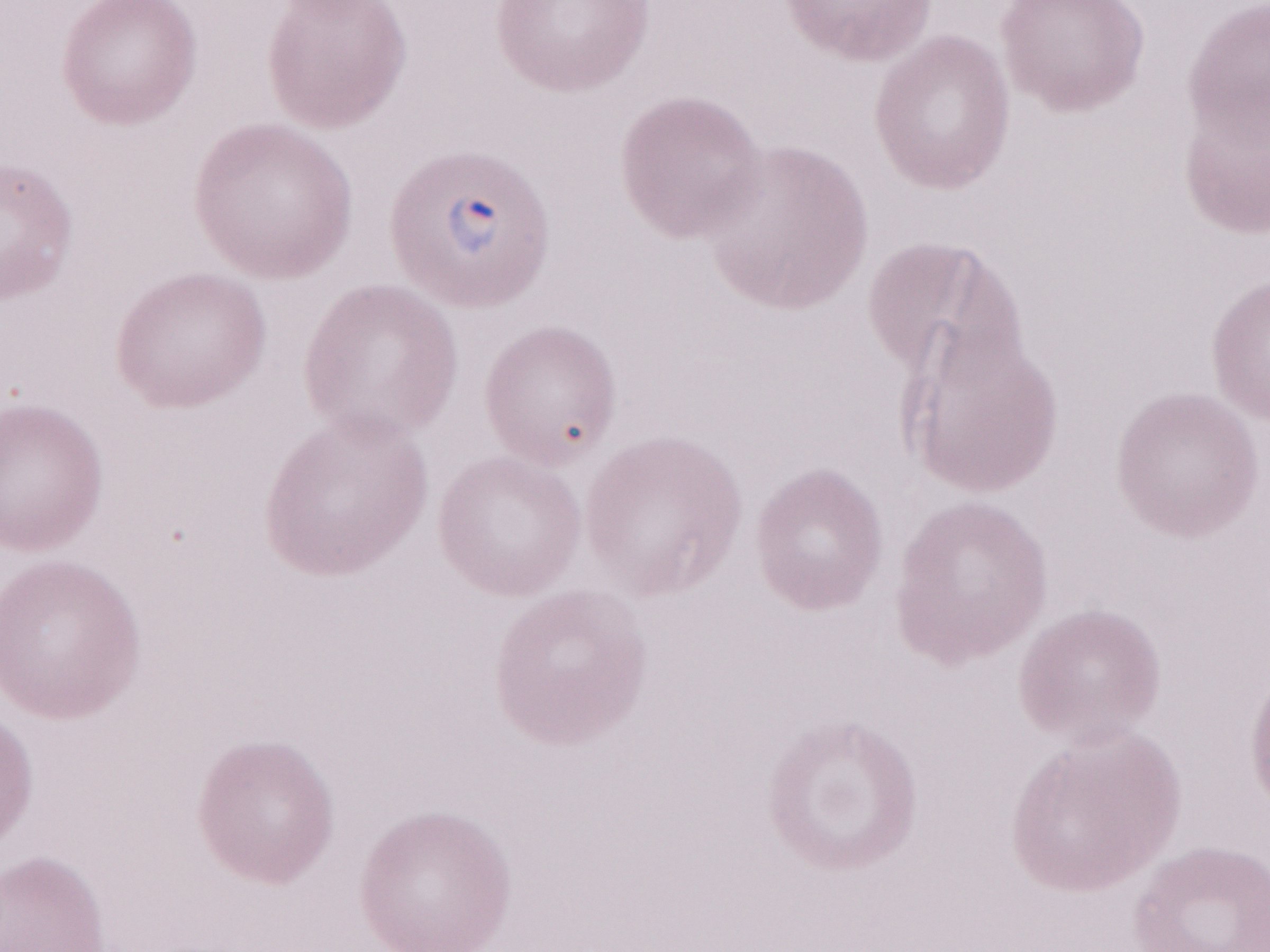 Patient-level malaria diagnosis: positive. May-Grünwald-Giemsa-stained preparation. Olympus BX43 microscope, Olympus DP73 camera. Single field of view. Thin peripheral-blood smear. Image is 1270×952 pixels. Magnification: 1,000x.